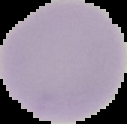
preparation = thin blood smear
result = negative for Plasmodium parasites
image size = 127×124 pixels
image type = segmented cell region on a black background